Give the position of every leukocyte visible.
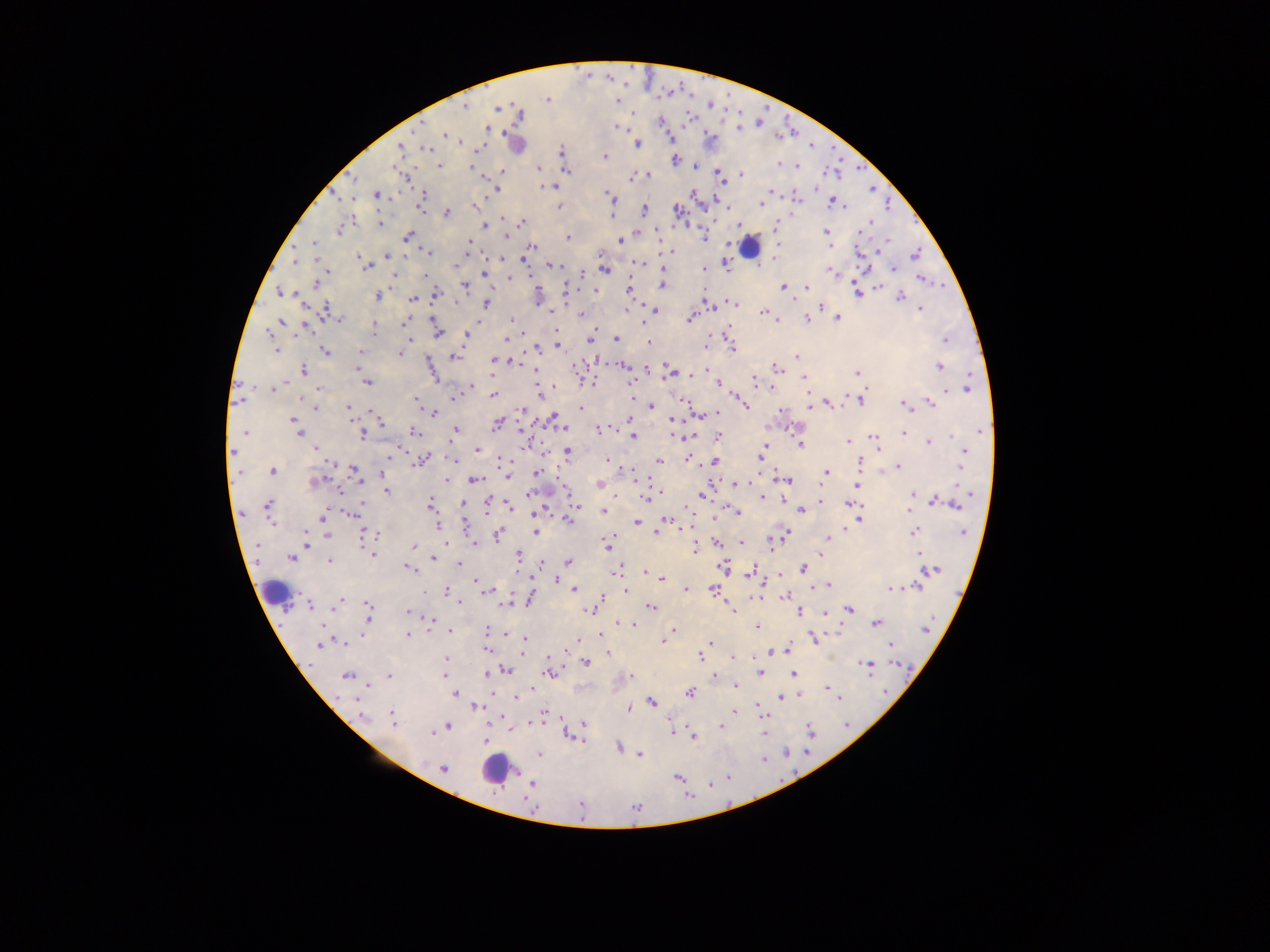
Approximate centers as x y in pixels.
Leukocytes: 750 246; 275 590; 492 770.

Malaria parasite locations: 547 99; 464 107; 498 107; 660 121; 420 126; 617 127; 739 128; 487 129; 444 135; 710 138; 669 139; 637 144; 426 148; 400 149; 562 150; 605 157; 675 160; 779 164; 439 165; 472 166; 796 166; 538 168; 567 171; 502 172; 647 175; 719 175; 742 175; 630 179; 546 186; 816 187; 494 189; 771 190; 693 194; 376 195; 422 195; 609 196; 797 199; 761 204; 834 204; 421 207; 558 207; 645 209; 678 211; 447 213; 612 215; 352 218; 504 219; 523 221; 380 224; 484 225; 775 227; 338 231; 826 231; 407 236; 704 237; 568 238; 468 241; 621 241; 313 243; 778 245; 530 248; 669 251; 428 253; 916 254; 386 255; 359 258; 523 259; 295 261; 459 263; 639 263; 366 266; 556 266; 725 266; 663 267; 894 269; 606 270; 704 270; 832 272; 484 273; 394 276; 510 278; 920 279; 316 285; 662 286; 784 286; 465 287; 807 287; 878 287; 630 289; 594 290; 566 291; 279 292; 857 292; 435 293; 377 296; 900 297; 413 299; 733 302; 456 303; 487 303; 708 303; 820 307; 655 309; 627 310; 920 310; 327 311; 553 311; 763 312; 767 314; 582 315; 837 317; 690 318; 339 319; 806 319; 281 320; 433 320; 511 320; 777 320; 406 322; 478 323; 304 327; 374 330; 556 331; 438 332; 268 333; 728 333; 466 335; 409 339; 505 339; 617 339; 589 340; 945 340; 649 343; 558 346; 536 349; 732 349; 275 351; 325 352; 359 352; 400 354; 454 357; 796 357; 358 361; 495 361; 517 363; 624 366; 939 367; 357 368; 777 368; 535 369; 303 370; 668 371; 698 371; 696 373; 857 373; 491 374; 804 378; 754 380; 367 382; 590 383; 718 384; 554 386; 473 387; 772 387; 967 388; 271 389; 319 389; 494 395; 454 398; 416 399; 738 399; 862 400; 829 403; 930 403; 810 405; 904 405; 746 406; 315 407; 347 407; 652 407; 582 408; 522 410; 433 413; 718 413; 375 414; 631 419; 291 420; 553 420; 673 420; 381 421; 497 424; 600 429; 455 430; 981 430; 414 431; 243 432; 903 433; 298 434; 361 435; 718 436; 633 437; 874 439; 847 442; 928 442; 800 444; 875 444; 315 448; 476 449; 232 452; 568 452; 963 452; 388 458; 759 458; 422 460; 502 460; 607 460; 687 460; 659 461; 715 462; 860 463; 961 463; 899 466; 354 470; 272 471; 382 472; 633 472; 537 473; 826 473; 508 476; 319 480; 474 480; 787 480; 447 481; 735 483; 599 484; 857 485; 387 491; 529 493; 913 494; 704 495; 762 497; 646 498; 783 500; 934 502; 430 504; 462 504; 850 504; 576 505; 957 505; 508 506; 268 507; 488 507; 801 510; 538 511; 909 511; 604 512; 736 512; 353 514; 322 518; 714 518; 666 520; 860 520; 568 521; 637 522; 438 526; 846 529; 536 532; 914 532; 963 532; 306 533; 656 533; 365 534; 327 535; 377 535; 784 535; 498 536; 828 537; 306 540; 741 542; 445 543; 474 543; 718 543; 607 546; 414 547; 695 548; 917 553; 372 554; 822 554; 519 556; 290 558; 433 558; 329 561; 569 562; 543 563; 459 564; 409 568; 619 568; 723 568; 804 569; 931 571; 615 572; 644 572; 752 572; 661 578; 556 580; 475 583; 829 585; 918 587; 891 588; 686 589; 575 590; 625 590; 711 590; 485 591; 447 592; 786 597; 530 599; 458 602; 338 603; 309 605; 368 607; 651 608; 731 609; 588 610; 849 610; 407 612; 800 612; 826 613; 368 615; 432 619; 876 624; 633 626; 757 627; 925 630; 450 631; 487 631; 673 631; 407 635; 600 636; 577 639; 813 639; 525 640; 663 640; 344 643; 711 643; 891 644; 319 645; 786 649; 772 652; 607 653; 699 657; 734 657; 446 659; 585 663; 867 665; 506 670; 760 672; 487 674; 549 674; 793 674; 444 675; 346 676; 389 676; 714 676; 631 677; 368 686; 736 686; 828 688; 690 692; 455 694; 798 695; 837 696; 517 697; 781 698; 652 702; 477 707; 630 707; 734 712; 544 714; 362 716; 393 720; 584 723; 447 726; 721 727; 809 729; 511 730; 671 731; 433 733; 567 735; 694 737; 485 738; 619 748; 539 754; 640 754; 443 769; 677 777; 531 785. Thick blood film. Image is 1270×952 pixels. One field of view. Collected in Ghana. Photographed through a microscope with a mobile-phone camera.